Outline each Plasmodium vivax-infected red blood cell.
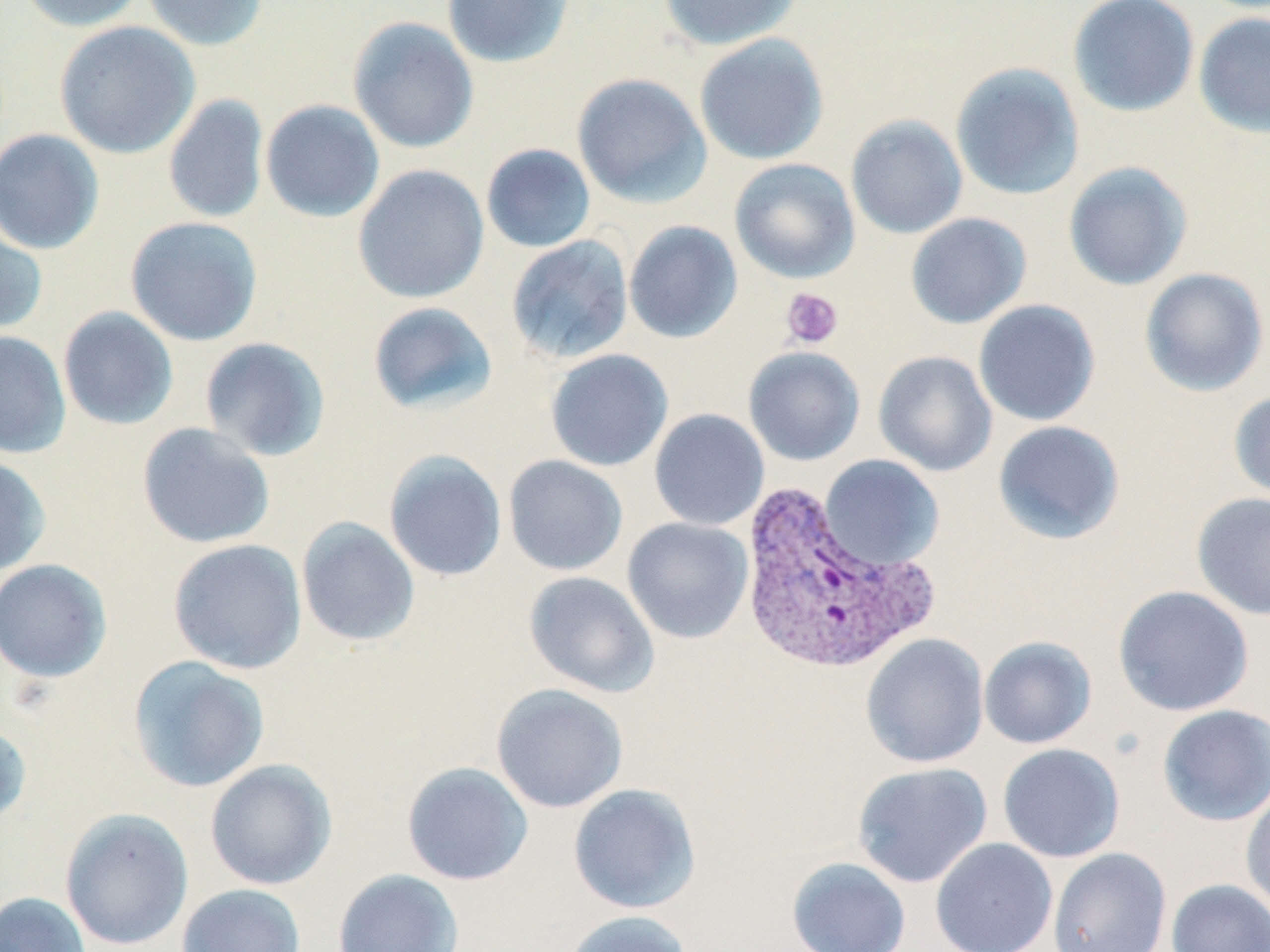
Approximate bounding boxes as [x1, y1, x2, y2] in pixels.
Plasmodium vivax-infected red blood cells: [737, 480, 939, 676].

Uninfected red blood cell locations: [16, 0, 147, 32], [141, 0, 269, 51], [441, 0, 575, 68], [658, 0, 802, 51], [1067, 0, 1199, 117], [1193, 12, 1270, 139], [347, 16, 479, 154], [54, 21, 200, 159], [694, 33, 829, 165], [950, 63, 1085, 201], [571, 73, 711, 207], [163, 94, 270, 224], [260, 99, 385, 223], [845, 114, 968, 239], [0, 128, 105, 255], [481, 144, 596, 253], [729, 158, 860, 284], [1063, 161, 1194, 291], [352, 164, 489, 304], [905, 212, 1032, 329], [125, 216, 263, 346], [0, 220, 48, 337], [623, 221, 743, 344], [505, 235, 634, 364], [1139, 267, 1269, 397], [973, 299, 1101, 427], [366, 301, 499, 416], [58, 306, 179, 431], [0, 330, 72, 458], [199, 336, 331, 462], [743, 347, 865, 466], [544, 349, 673, 472], [873, 350, 997, 477], [1228, 391, 1270, 505], [649, 408, 770, 531], [992, 420, 1125, 544], [136, 422, 275, 549], [383, 450, 507, 582], [0, 454, 51, 577], [503, 455, 628, 576], [819, 455, 944, 571], [1191, 491, 1270, 622], [296, 517, 420, 648], [622, 517, 754, 644], [167, 538, 308, 674], [0, 559, 113, 683], [523, 571, 659, 698], [1113, 585, 1254, 716], [860, 633, 989, 769], [978, 636, 1097, 749], [127, 656, 270, 793], [491, 683, 629, 813], [1157, 704, 1270, 827], [0, 722, 32, 826], [997, 743, 1126, 863], [205, 759, 338, 890], [401, 761, 534, 886], [852, 762, 993, 888], [568, 783, 702, 914], [1240, 788, 1270, 916], [60, 808, 194, 950], [930, 837, 1058, 952], [1048, 847, 1172, 952], [787, 857, 911, 952], [331, 869, 465, 952], [1166, 879, 1270, 952], [177, 883, 306, 952], [0, 891, 91, 952], [561, 910, 693, 952]. Platelet locations: [781, 287, 843, 350]. Slide-level diagnosis: Plasmodium vivax. Image is 1270×952 pixels. May-Grünwald-Giemsa stain. One field of a larger specimen. Captured at 1000x magnification. Thin blood film. Light microscopy.